Identify the parasite.
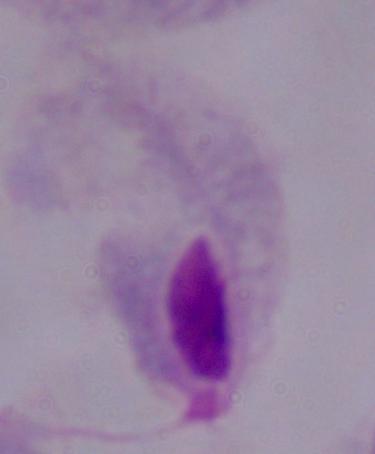

This is a trichomonad.

Summary:
  - Modality: photomicrograph
  - Magnification: 1000x